Assess this cell for malaria.
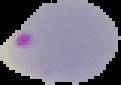
It is parasitized.

Summary:
  - Preparation: thin blood smear
  - Image size: 121×85 pixels
  - Image type: segmented cell region on a black background